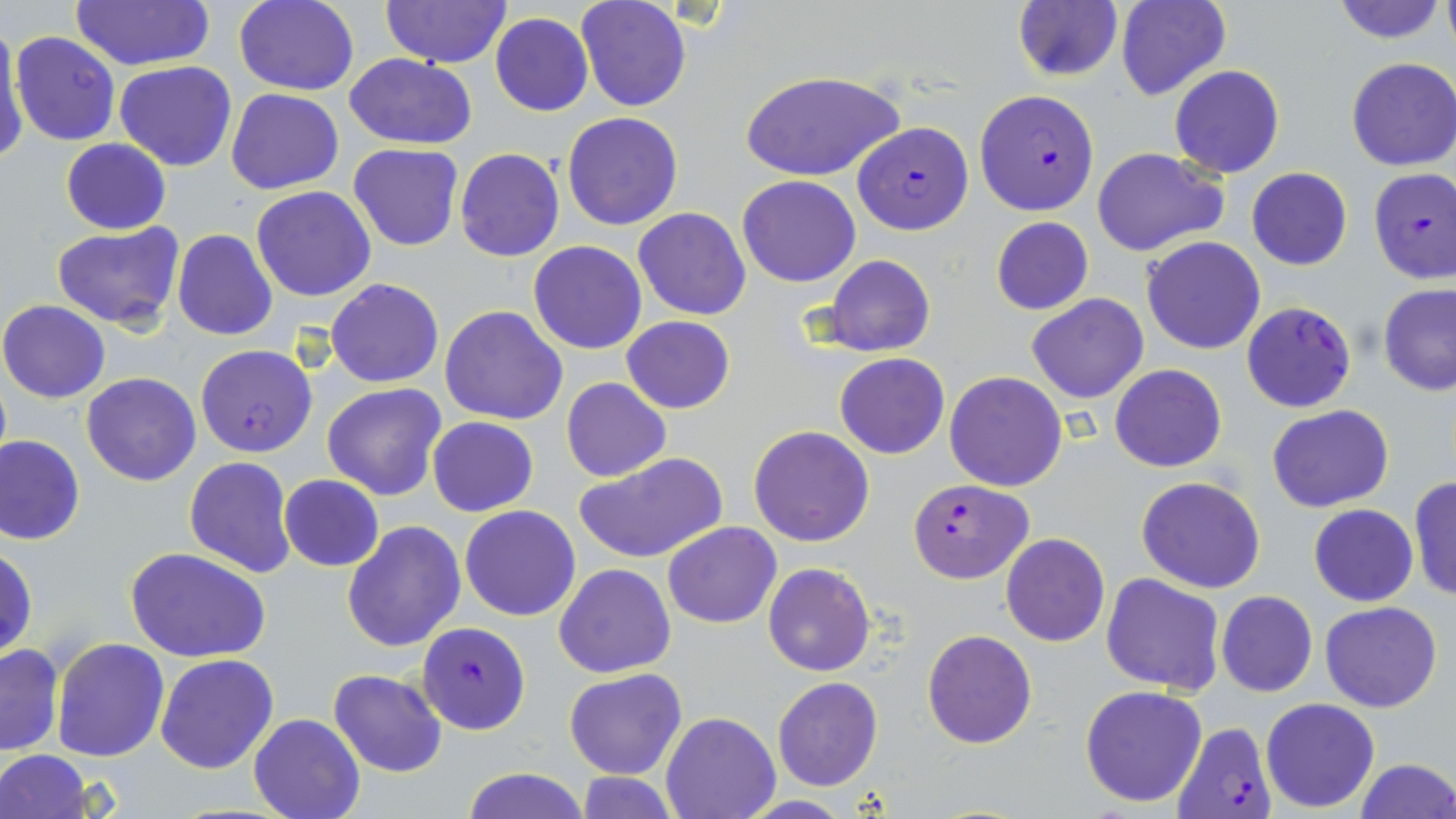 Approximate bounding boxes as [x1, y1, x2, y2] in pixels. Plasmodium falciparum-infected red blood cell locations: [974, 89, 1100, 215], [852, 121, 974, 235], [1368, 169, 1456, 285], [1241, 301, 1357, 413], [195, 344, 317, 457], [906, 478, 1033, 582], [416, 621, 531, 735], [1171, 720, 1278, 819]. Uninfected red blood cell locations: [235, 0, 359, 96], [381, 0, 511, 68], [576, 0, 691, 112], [1115, 0, 1229, 101], [1331, 0, 1447, 45], [1442, 0, 1456, 57], [69, 1, 216, 70], [1012, 2, 1122, 81], [491, 13, 594, 116], [0, 24, 25, 162], [11, 33, 121, 146], [345, 54, 478, 149], [1346, 58, 1456, 171], [114, 61, 235, 170], [1170, 65, 1285, 179], [740, 70, 900, 183], [227, 90, 345, 194], [562, 111, 683, 231], [60, 138, 170, 234], [349, 143, 463, 251], [454, 147, 564, 262], [1092, 148, 1229, 258], [1245, 167, 1352, 270], [737, 174, 861, 287], [251, 186, 377, 302], [634, 207, 751, 319], [991, 217, 1093, 314], [51, 222, 186, 330], [172, 230, 277, 341], [1142, 235, 1266, 354], [529, 240, 647, 354], [824, 254, 935, 358], [326, 277, 443, 387], [1379, 283, 1456, 396], [1026, 294, 1148, 404], [0, 299, 109, 403], [439, 305, 568, 425], [621, 317, 735, 414], [834, 353, 950, 459], [1110, 365, 1226, 472], [944, 371, 1068, 492], [81, 373, 201, 486], [562, 377, 670, 482], [322, 383, 447, 502], [1267, 404, 1394, 512], [428, 417, 539, 516], [748, 425, 875, 548], [0, 434, 85, 544], [574, 451, 727, 566], [184, 456, 296, 578], [1136, 474, 1266, 593], [279, 475, 383, 572], [1407, 475, 1456, 601], [1309, 504, 1418, 606], [459, 505, 581, 621], [342, 519, 467, 651], [663, 522, 782, 628], [1000, 532, 1110, 646], [1, 545, 37, 660], [124, 546, 272, 663], [554, 564, 675, 678], [763, 564, 877, 677], [1100, 572, 1225, 693], [1217, 591, 1317, 698], [1319, 602, 1442, 713], [922, 629, 1036, 748], [51, 637, 170, 761], [0, 643, 63, 756], [154, 654, 279, 774], [328, 668, 447, 778], [564, 668, 687, 780], [773, 677, 882, 791], [1079, 684, 1207, 808], [1261, 697, 1379, 812], [661, 711, 780, 818], [248, 713, 364, 819], [0, 751, 93, 819], [1353, 758, 1456, 818], [461, 766, 588, 819], [574, 774, 682, 817]. Slide-level diagnosis: Plasmodium falciparum. Thin blood smear. Image is 1456×819 pixels. 1000x magnification. Light microscopy. Single field of view. May-Grünwald-Giemsa-stained preparation.